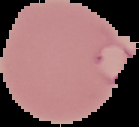

malaria status = parasitized
image type = segmented cell region with the area outside set to black
image size = 139×127 pixels
preparation = thin blood smear